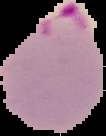

Summary:
  - Result: malaria parasites detected
  - Image size: 106×136 pixels
  - Preparation: thin blood smear
  - Image type: segmented cell region on a black background